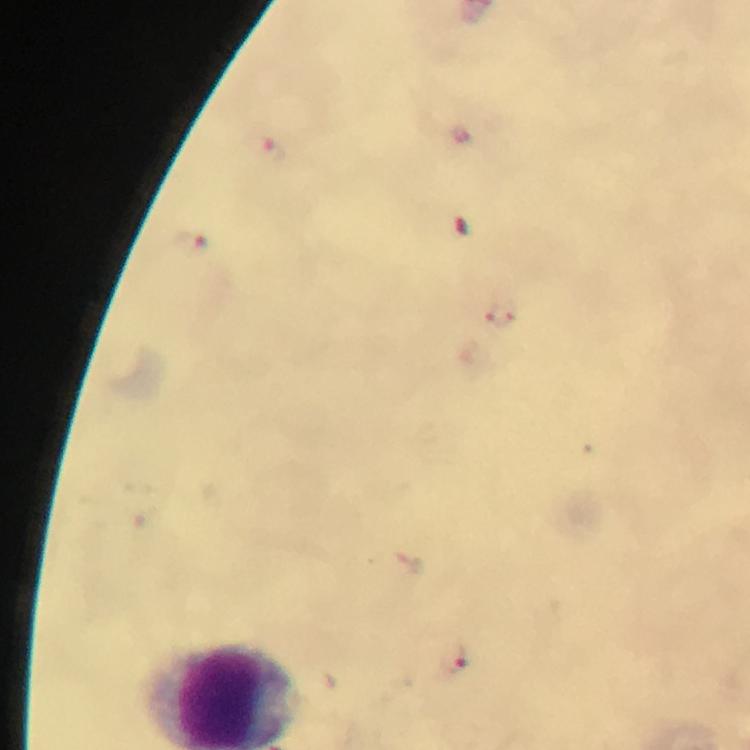 Approximate object centers, in pixels from the top-left corner. Plasmodium parasite locations: (x=272, y=151), (x=189, y=241), (x=503, y=314), (x=453, y=661). Giemsa stain. From a diagnostic examination for malaria. Image is 750×750 pixels. A crop from one field of view. Photographed through the microscope with a smartphone camera. Thick blood film. At 100x magnification. Immersion oil applied.